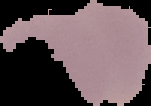
Image is 151×106 pixels. Result: no Plasmodium parasites detected. From a thin blood film. The area outside the segmented cell region is set to black.